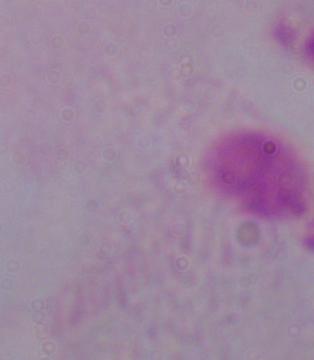

A trichomonad is seen. 1000x magnification. Micrograph.